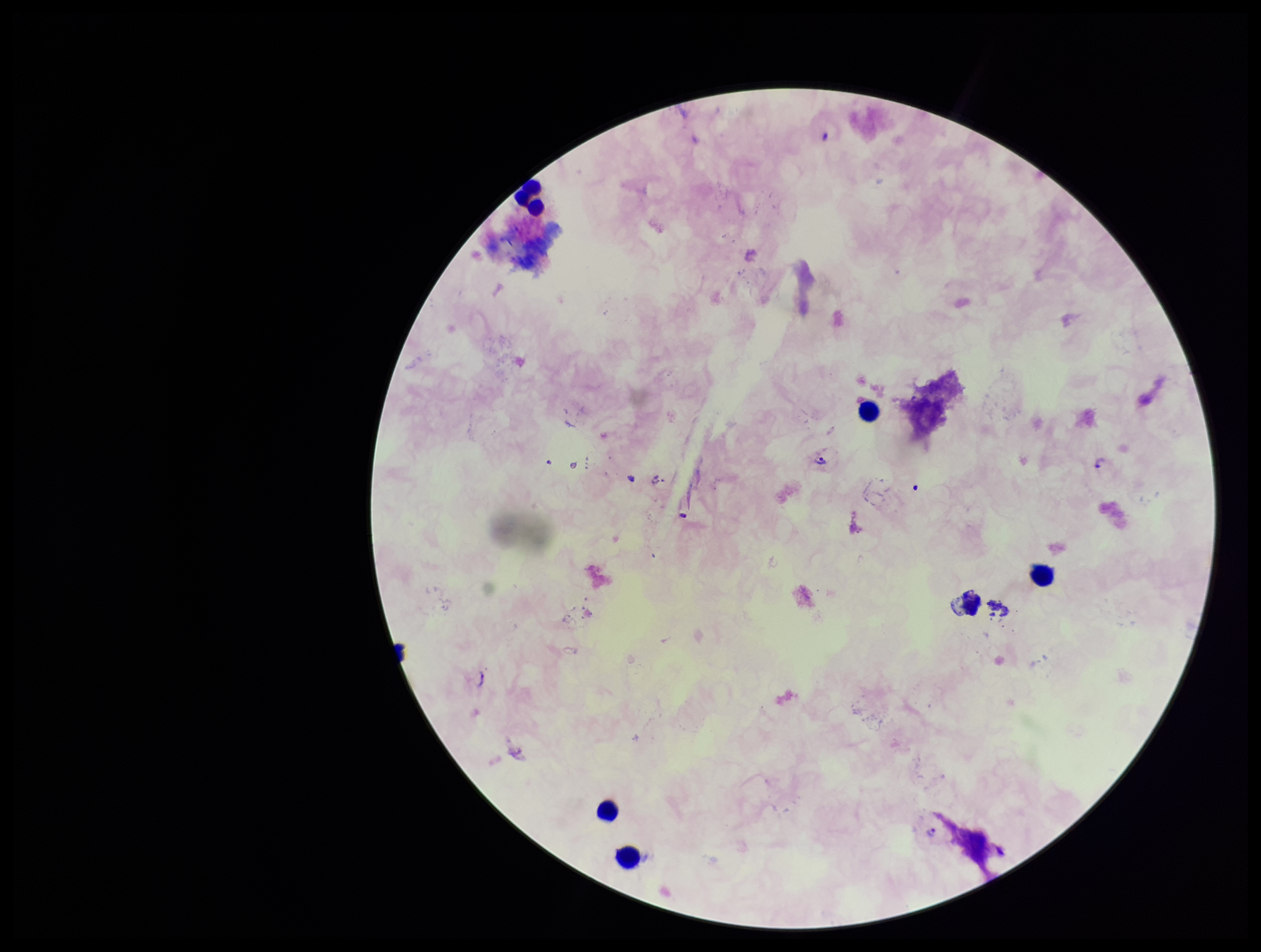
Single field of view. Leukocyte count: 5. Patient malaria status: infected. Stained with Giemsa. Species reported for this patient: Plasmodium falciparum. Plasmodium parasites: identified. Smartphone photograph taken through the eyepiece of a microscope. Image is 1261×952 pixels. Parasite count: 2. Preparation: thick.